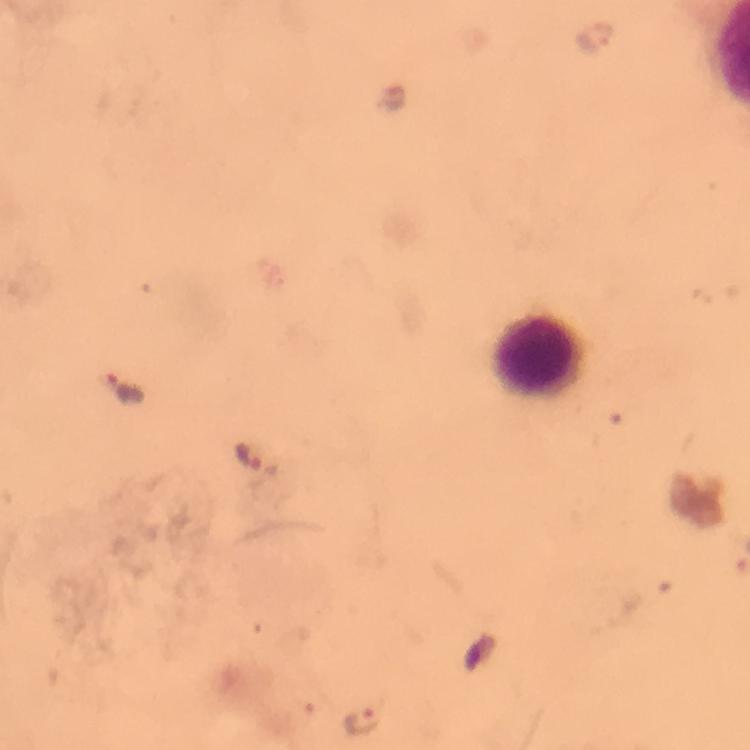
cropped from = a single field of view
magnification = 100x
malaria parasite locations = approximate centers as (x, y) in pixels: (594, 37), (396, 96), (123, 384), (246, 456), (363, 723)
preparation = thick blood smear
stain = Giemsa
immersion oil = applied
context = from a diagnostic examination for malaria
capture = smartphone camera through the microscope
leukocyte locations = approximate centers as (x, y) in pixels: (532, 356)
image size = 750×750 pixels